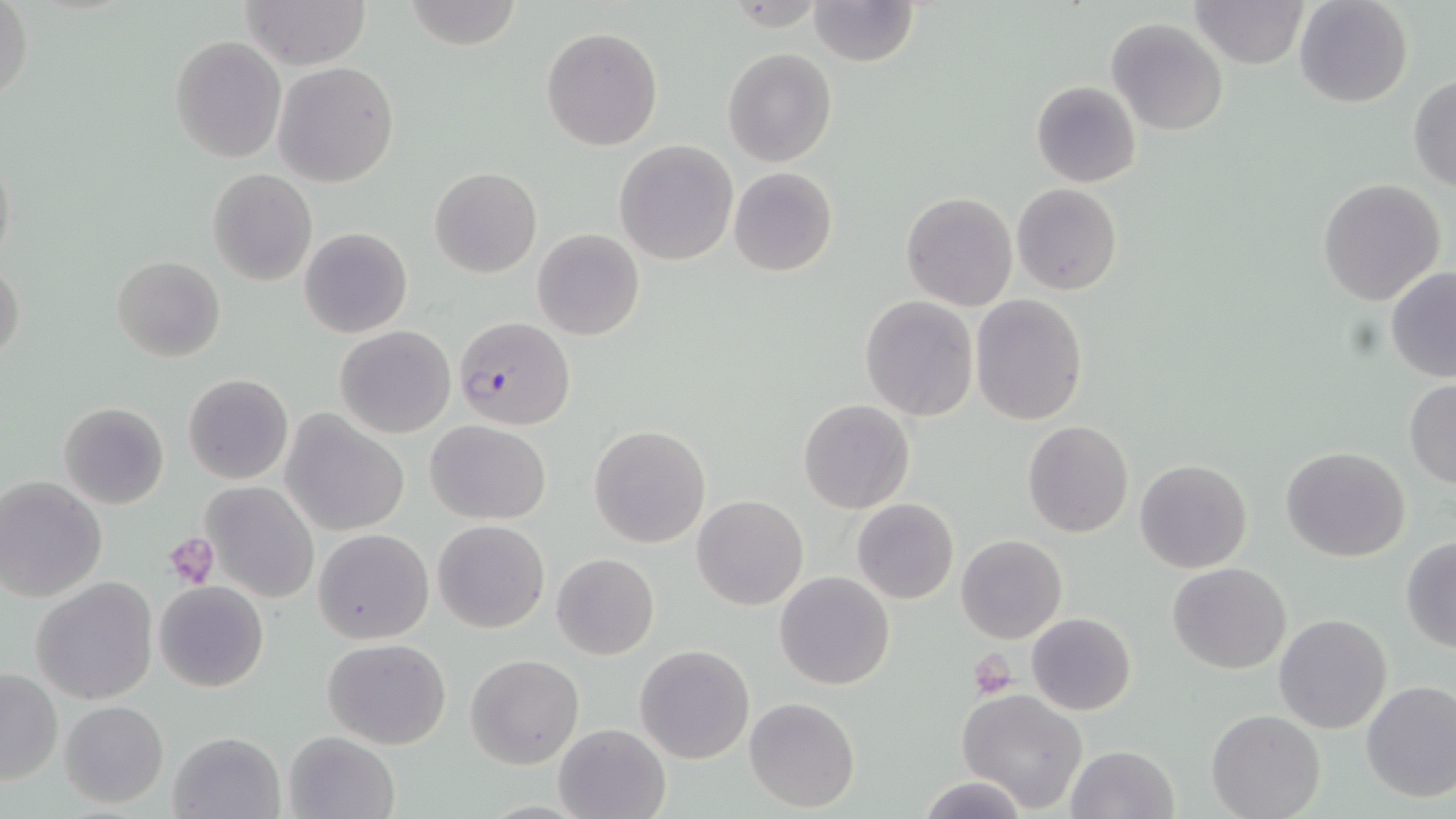 Approximate bounding boxes as (x1, y1, x2, y2) in pixels. Uninfected red blood cell locations: (241, 0, 369, 69), (404, 0, 526, 50), (809, 0, 917, 66), (1191, 0, 1308, 69), (1293, 0, 1414, 110), (1, 1, 31, 108), (1107, 19, 1228, 136), (541, 25, 664, 150), (169, 36, 286, 161), (722, 48, 837, 167), (273, 61, 399, 186), (1408, 74, 1455, 192), (1031, 80, 1142, 188), (614, 139, 740, 265), (1, 143, 16, 275), (430, 166, 541, 277), (727, 167, 839, 277), (208, 168, 318, 285), (1316, 178, 1445, 306), (1012, 183, 1122, 294), (901, 192, 1017, 312), (299, 227, 413, 339), (532, 229, 644, 341), (112, 254, 225, 362), (0, 260, 26, 367), (1386, 268, 1456, 381), (970, 295, 1089, 426), (860, 296, 979, 422), (335, 325, 456, 438), (183, 373, 293, 485), (1404, 379, 1456, 488), (798, 399, 916, 515), (59, 401, 169, 510), (283, 414, 410, 537), (427, 419, 550, 525), (1023, 420, 1133, 537), (589, 425, 711, 548), (1281, 446, 1409, 562), (1135, 458, 1252, 574), (0, 476, 107, 601), (203, 481, 321, 602), (692, 495, 808, 611), (853, 498, 959, 604), (434, 519, 549, 634), (313, 528, 434, 643), (956, 533, 1067, 644), (1401, 538, 1456, 652), (551, 553, 659, 660), (1167, 561, 1292, 675), (775, 571, 895, 690), (30, 576, 159, 705), (155, 581, 269, 692), (1026, 612, 1135, 716), (1273, 613, 1394, 734), (322, 638, 452, 750), (635, 644, 755, 765), (466, 654, 584, 769), (0, 668, 62, 785), (1360, 681, 1456, 804), (957, 688, 1089, 814), (744, 697, 861, 812), (60, 700, 168, 807), (1205, 709, 1326, 819), (553, 722, 671, 819), (167, 730, 285, 819), (282, 730, 399, 819), (1065, 745, 1178, 819), (918, 775, 1029, 819). Plasmodium falciparum-infected red blood cell locations: (454, 315, 576, 430). Platelet locations: (164, 532, 220, 588), (968, 653, 1017, 697). Slide-level diagnosis: Plasmodium falciparum. Image is 1456×819 pixels. May-Grünwald-Giemsa-stained preparation. Thin blood smear. Optical microscopy. One field of a larger specimen. Captured at 1000x magnification.